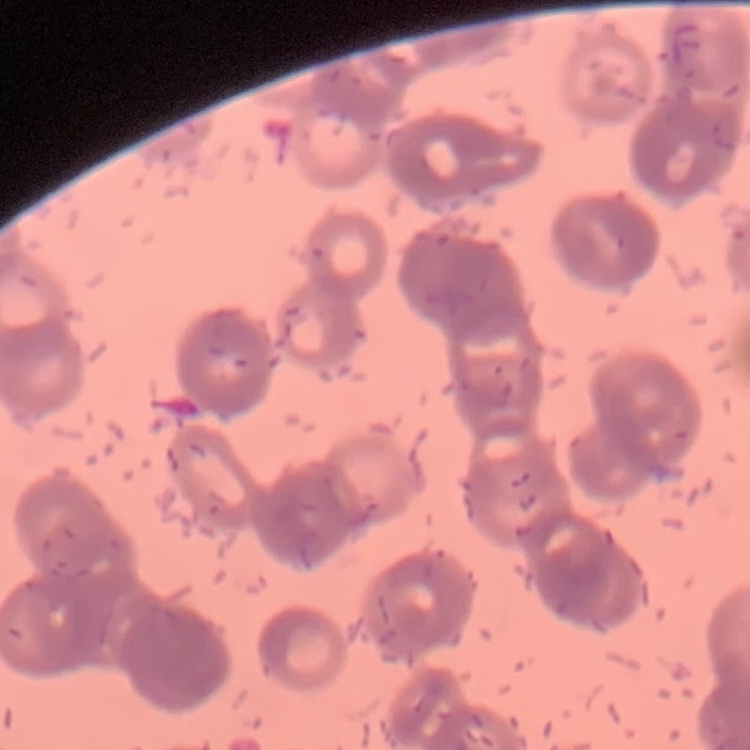
erythrocyte morphology = rouleaux formation
preparation = thin blood film
stain = Field's or Giemsa
image type = square crop of a larger photomicrograph